Classify this cell by malaria status.
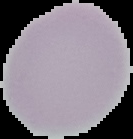

Uninfected.

From a thin blood smear. Image is 133×139 pixels. The area outside the segmented cell region is set to black.